Give the position of each Plasmodium falciparum parasite with its life-cycle stage, each leukocyte, and any debris.
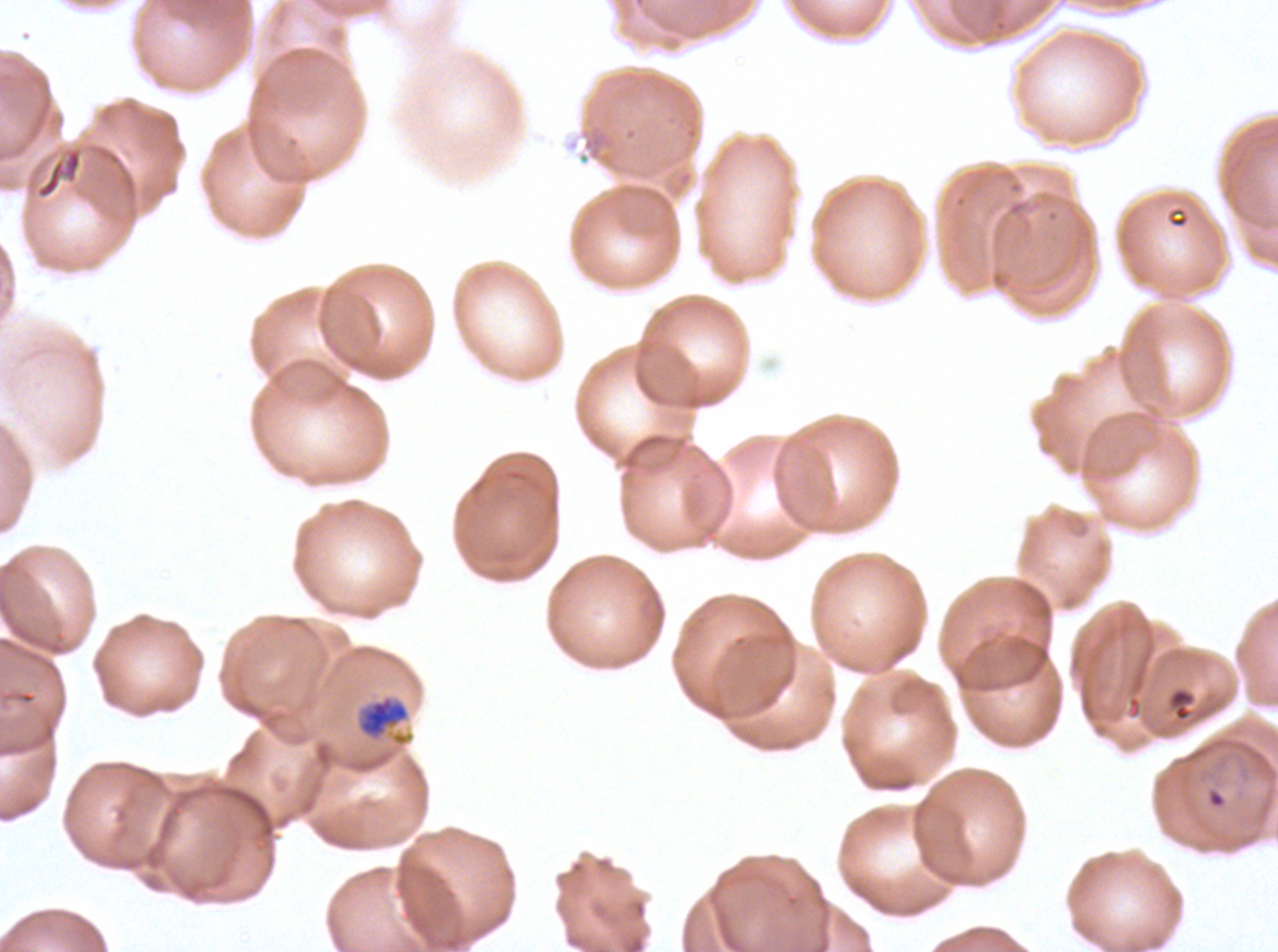
Approximate bounding boxes as {x1, y1, x2, y2} in pixels.
Rings: {1207, 789, 1226, 809}.
Mid trophozoites: {358, 695, 410, 738}.
No late-ring/early-trophozoite forms, late trophozoites, early schizonts, late schizonts, segmenters, gametocytes, leukocytes, or debris observed.

Thin blood film. One sub-image of a larger composite. Life-cycle stages observed: ring, mid trophozoite. Ex-vivo Plasmodium falciparum culture from a patient in The Gambia, grown for 24 to 48 hours. Giemsa-stained preparation. Image is 1278×952 pixels.